Assess this cell for malaria.
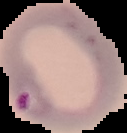

It is parasitized.

image size = 127×133 pixels
preparation = thin blood film
image type = segmented cell region on a black background